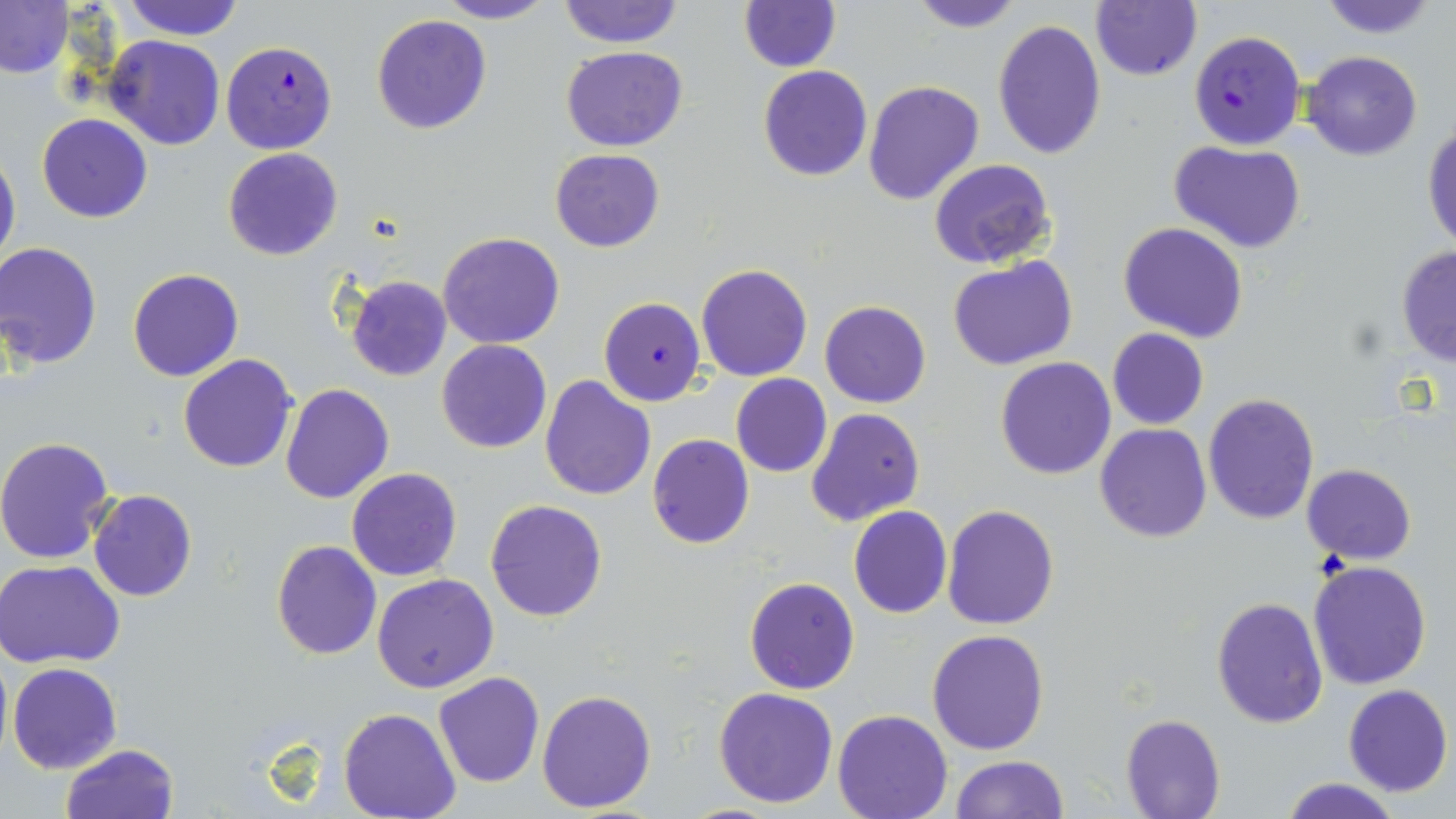
Summary:
  - Coordinate format: approximate bounding boxes as (x1, y1, x2, y2) in pixels
  - Uninfected red blood cell locations: (120, 0, 243, 40), (436, 0, 554, 25), (556, 0, 685, 47), (906, 0, 1023, 32), (1316, 0, 1441, 38), (0, 1, 73, 79), (737, 1, 841, 72), (1089, 1, 1202, 82), (370, 14, 492, 133), (992, 21, 1107, 160), (103, 35, 226, 150), (560, 45, 688, 151), (1303, 50, 1421, 160), (757, 65, 872, 181), (863, 80, 984, 206), (37, 113, 152, 223), (1423, 123, 1455, 255), (1170, 140, 1307, 255), (222, 147, 344, 261), (0, 148, 20, 273), (549, 148, 665, 252), (929, 159, 1055, 269), (1119, 222, 1249, 343), (437, 231, 566, 348), (0, 242, 102, 369), (1395, 246, 1456, 366), (949, 256, 1078, 370), (696, 263, 813, 382), (128, 268, 243, 382), (343, 275, 452, 383), (819, 300, 931, 408), (1106, 329, 1209, 429), (436, 339, 553, 454), (178, 354, 299, 473), (995, 356, 1116, 478), (730, 373, 832, 477), (539, 374, 656, 500), (280, 382, 394, 503), (1203, 393, 1320, 525), (807, 408, 926, 527), (1095, 424, 1212, 544), (647, 433, 754, 549), (0, 436, 118, 565), (1302, 464, 1416, 563), (355, 466, 476, 688), (347, 467, 462, 581), (87, 490, 197, 602), (485, 498, 608, 622), (941, 504, 1061, 630), (848, 506, 952, 618), (271, 540, 381, 659), (1, 560, 127, 669), (1309, 560, 1432, 689), (372, 573, 500, 694), (744, 576, 859, 695), (1211, 595, 1328, 728), (927, 629, 1050, 755), (8, 661, 122, 774), (433, 672, 544, 788), (1343, 683, 1453, 797), (713, 687, 838, 808), (536, 688, 657, 813), (338, 709, 461, 819), (833, 710, 954, 819), (1121, 714, 1226, 818), (60, 744, 179, 819), (951, 755, 1069, 818), (1278, 776, 1403, 819)
  - Plasmodium falciparum-infected red blood cell locations: (1189, 30, 1305, 149), (220, 41, 338, 154), (599, 296, 707, 407)
  - Slide-level diagnosis: Plasmodium falciparum
  - Magnification: 1000x
  - Modality: optical microscopy
  - Image size: 1456×819 pixels
  - Field of view: single
  - Stain: May-Grünwald-Giemsa
  - Preparation: thin blood film